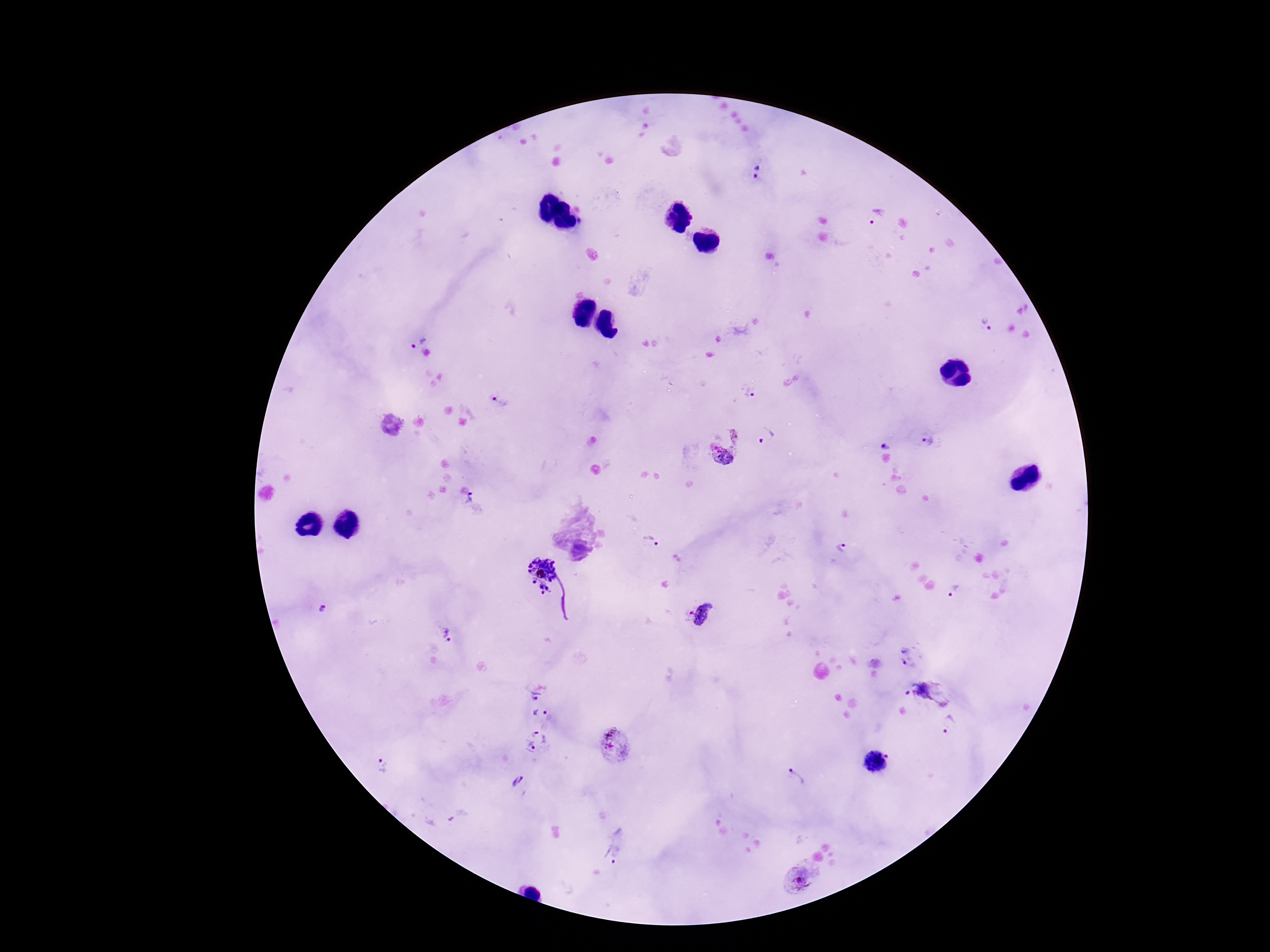

Approximate object centers, in pixels from the top-left corner.
Summary:
  - Plasmodium parasite locations: (x=758, y=172), (x=876, y=216), (x=986, y=325), (x=417, y=339), (x=748, y=393), (x=499, y=404), (x=766, y=436), (x=925, y=440), (x=888, y=444), (x=724, y=445), (x=474, y=504), (x=651, y=541), (x=843, y=550), (x=540, y=575), (x=952, y=592), (x=324, y=608), (x=701, y=613), (x=445, y=634), (x=909, y=657), (x=926, y=695), (x=536, y=696), (x=540, y=714), (x=949, y=724), (x=538, y=741), (x=613, y=745), (x=877, y=761), (x=384, y=767), (x=796, y=777), (x=518, y=781), (x=618, y=845), (x=797, y=879)
  - Field of view: single
  - Patient malaria status: infected
  - Image size: 1270×952 pixels
  - Preparation: thick peripheral-blood smear
  - Magnification: 100x
  - Capture: smartphone camera through the microscope eyepiece
  - Stain: Giemsa